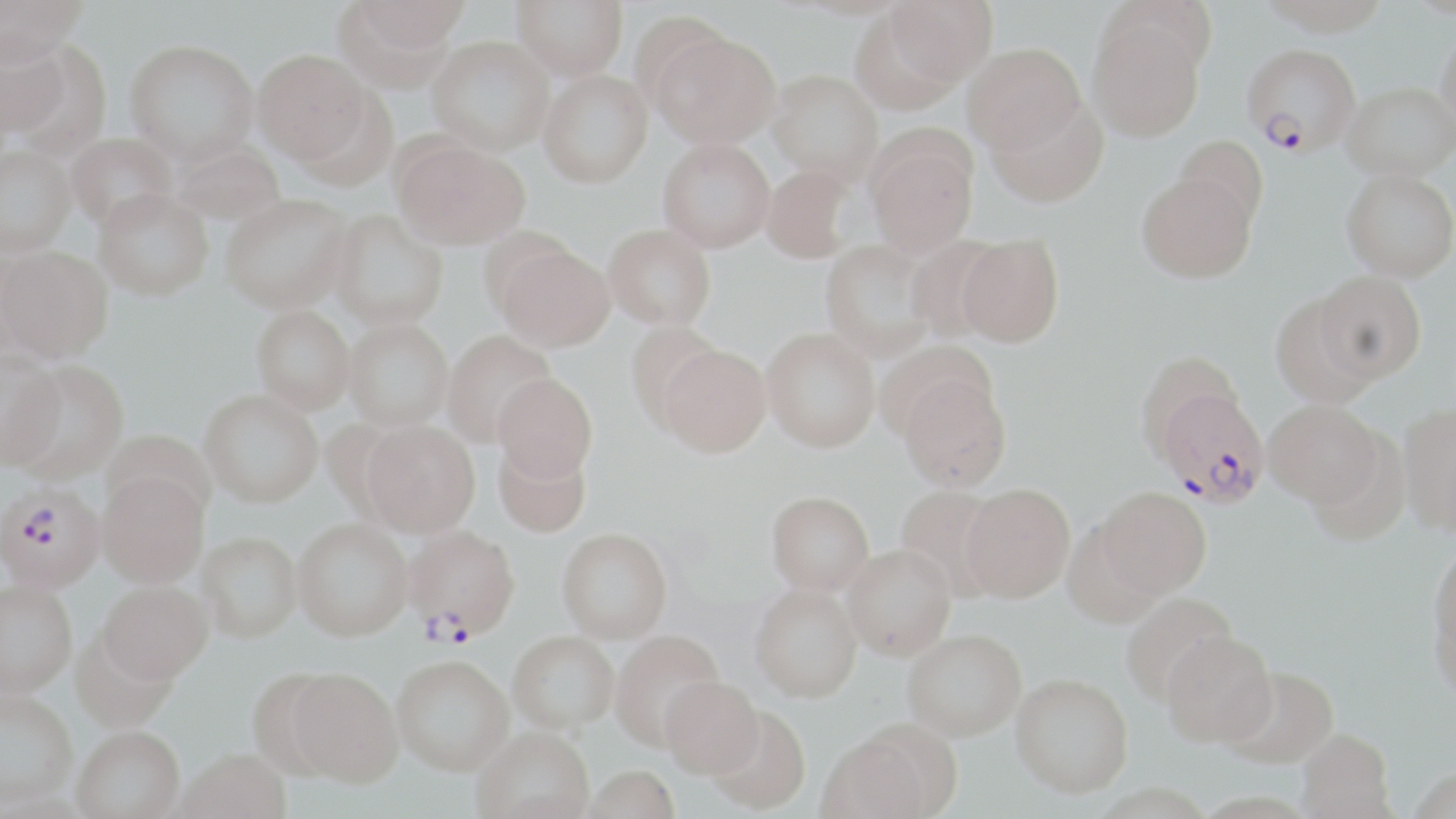
slide_level_diagnosis: Plasmodium falciparum
stain: May-Grünwald-Giemsa
plasmodium_falciparum_infected_red_blood_cell_locations: 'approximate bounding boxes as (x1,y1)-(x2,y2) corner pairs in pixels: (1237,49)-(1355,157), (1153,387)-(1270,507), (0,482)-(105,592), (403,525)-(519,646)'
magnification: 1000x
modality: light microscopy
uninfected_red_blood_cell_locations: 'approximate bounding boxes as (x1,y1)-(x2,y2) corner pairs in pixels: (1,0)-(88,58), (349,0)-(469,54), (513,0)-(628,79), (883,0)-(997,89), (1086,11)-(1208,142), (1436,24)-(1456,134), (0,30)-(78,146), (653,31)-(781,148), (427,35)-(554,156), (125,38)-(259,165), (962,42)-(1085,154), (252,49)-(370,164), (539,69)-(653,188), (767,69)-(883,187), (1343,81)-(1456,180), (986,97)-(1109,206), (66,132)-(178,232), (1172,135)-(1269,232), (867,137)-(977,258), (658,138)-(775,252), (395,139)-(530,250), (170,142)-(286,226), (0,144)-(75,255), (761,164)-(857,263), (1341,168)-(1456,281), (1137,172)-(1257,282), (93,188)-(213,300), (220,193)-(354,314), (329,209)-(448,330), (603,224)-(716,330), (956,234)-(1064,347), (820,239)-(938,359), (496,244)-(615,351), (1,246)-(111,362), (1314,270)-(1427,384), (1270,296)-(1379,408), (251,305)-(355,413), (343,318)-(454,430), (629,323)-(730,431), (761,327)-(880,452), (441,330)-(556,446), (658,343)-(770,456), (1135,349)-(1244,458), (0,350)-(66,468), (7,359)-(130,482), (494,373)-(597,482), (897,373)-(1011,492), (199,389)-(323,507), (1263,399)-(1383,508), (1398,403)-(1456,535), (361,420)-(480,537), (101,429)-(217,524), (493,439)-(591,538), (96,472)-(208,588), (961,483)-(1075,602), (896,485)-(1007,596), (1096,487)-(1211,598), (766,490)-(874,594), (293,518)-(412,641), (556,527)-(673,642), (197,531)-(302,642), (1430,541)-(1456,664), (842,543)-(956,660), (0,579)-(78,698), (98,580)-(213,685), (750,583)-(862,701), (1121,592)-(1239,705), (1431,595)-(1456,710), (903,629)-(1026,740), (71,630)-(178,733), (507,630)-(619,733), (609,630)-(724,751), (1160,630)-(1277,748), (392,654)-(513,775), (1221,665)-(1338,767), (284,668)-(404,788), (246,669)-(350,782), (1010,673)-(1133,797), (660,676)-(762,777), (0,690)-(78,809), (707,704)-(811,814), (470,727)-(595,819), (72,728)-(185,819), (1296,728)-(1395,819), (818,731)-(937,819), (175,751)-(292,819), (582,765)-(680,819)'
field_of_view: one of a larger specimen
image_size: 1456×819 pixels
preparation: thin blood film